Find the cells and give the type of each one.
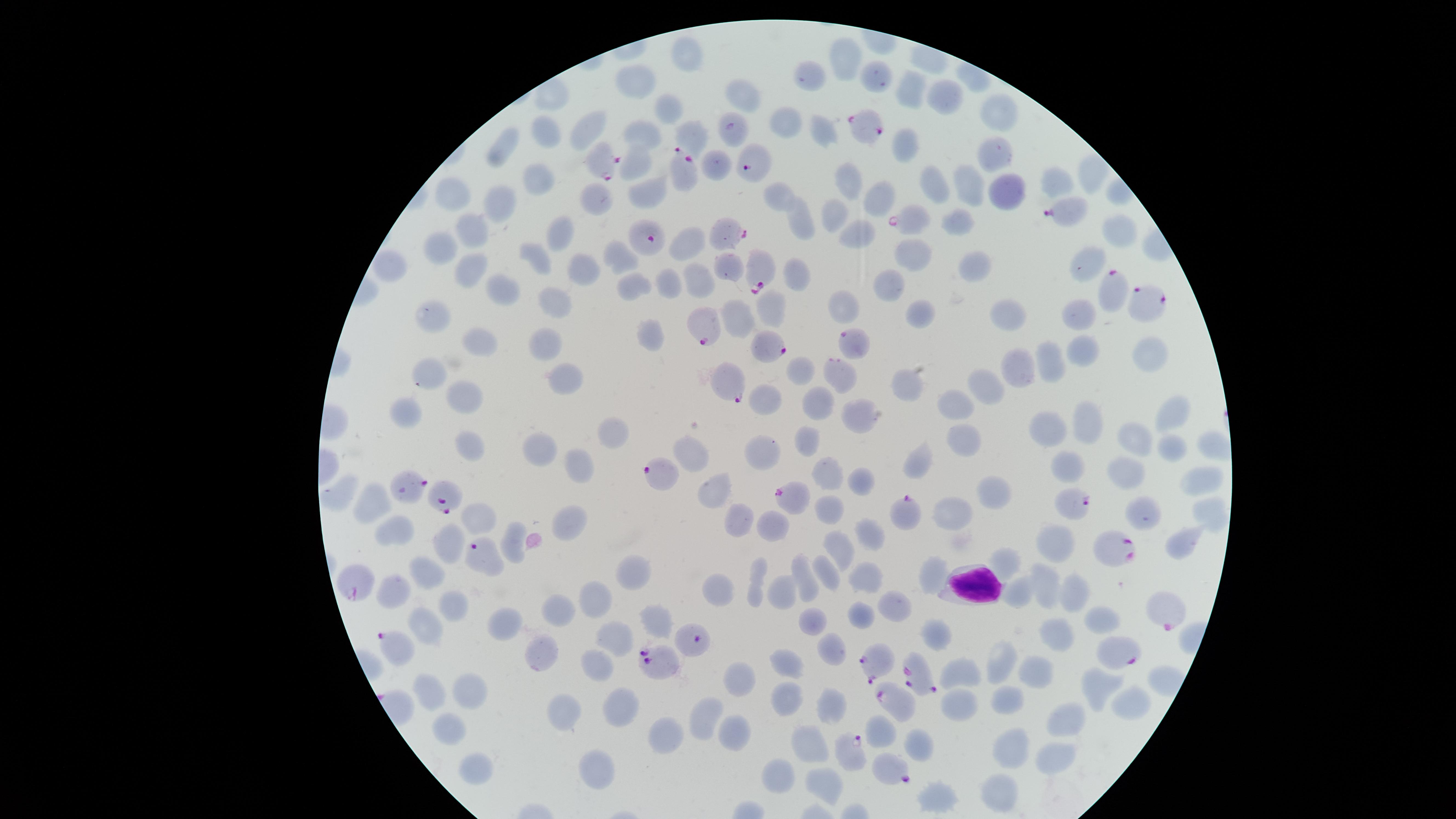

Approximate marker points as {x, y} in pixels.
Parasitized RBCs: {869, 131}, {604, 160}, {752, 164}, {686, 173}, {1066, 211}, {909, 219}, {728, 232}, {647, 238}, {759, 268}, {1111, 295}, {1157, 301}, {707, 328}, {767, 344}, {853, 344}, {838, 368}, {729, 383}, {408, 488}, {789, 495}, {440, 502}, {1072, 505}, {905, 513}, {1113, 550}, {481, 554}, {359, 587}, {1161, 604}, {392, 644}, {1113, 646}, {873, 661}, {656, 662}, {916, 678}, {893, 699}, {847, 744}, {888, 765}.
Uninfected RBCs: {687, 57}, {843, 57}, {870, 75}, {639, 80}, {810, 81}, {908, 94}, {941, 99}, {744, 101}, {669, 107}, {1004, 110}, {786, 124}, {586, 127}, {821, 131}, {643, 134}, {546, 135}, {696, 136}, {902, 145}, {505, 149}, {996, 151}, {639, 158}, {531, 181}, {1056, 181}, {845, 184}, {963, 186}, {930, 188}, {1006, 188}, {646, 191}, {777, 191}, {452, 194}, {596, 198}, {504, 200}, {876, 201}, {833, 215}, {964, 218}, {804, 224}, {475, 229}, {1118, 234}, {558, 236}, {858, 236}, {690, 248}, {440, 249}, {909, 256}, {533, 257}, {615, 257}, {584, 265}, {726, 266}, {976, 266}, {1090, 266}, {394, 268}, {475, 270}, {798, 275}, {701, 279}, {635, 284}, {670, 284}, {891, 284}, {504, 289}, {553, 299}, {843, 305}, {769, 310}, {1082, 312}, {434, 314}, {1001, 314}, {917, 315}, {741, 317}, {479, 340}, {546, 342}, {651, 343}, {1078, 346}, {1144, 354}, {1055, 356}, {802, 367}, {1015, 369}, {425, 372}, {567, 375}, {902, 385}, {988, 386}, {463, 397}, {764, 399}, {956, 399}, {814, 404}, {407, 410}, {858, 413}, {1163, 416}, {1082, 424}, {612, 429}, {1046, 431}, {1130, 435}, {807, 441}, {964, 441}, {1215, 441}, {469, 445}, {1169, 445}, {543, 447}, {761, 454}, {695, 457}, {576, 463}, {915, 466}, {1070, 469}, {1127, 473}, {830, 477}, {1203, 480}, {862, 482}, {714, 493}, {335, 495}, {990, 495}, {376, 507}, {829, 508}, {943, 513}, {473, 515}, {1140, 516}, {1214, 516}, {742, 520}, {574, 522}, {771, 522}, {400, 531}, {873, 536}, {1185, 539}, {513, 540}, {445, 545}, {1054, 545}, {840, 548}, {1006, 563}, {831, 569}, {636, 573}, {424, 574}, {934, 574}, {868, 579}, {758, 582}, {810, 582}, {1043, 584}, {785, 588}, {720, 590}, {397, 592}, {596, 592}, {1019, 593}, {1071, 593}, {893, 605}, {463, 607}, {565, 610}, {1097, 616}, {657, 617}, {862, 617}, {814, 621}, {508, 624}, {423, 626}, {1059, 633}, {613, 634}, {938, 636}, {835, 648}, {545, 653}, {1008, 660}, {788, 661}, {596, 665}, {1037, 668}, {965, 675}, {742, 678}, {1095, 687}, {472, 691}, {788, 693}, {437, 695}, {1131, 702}, {1008, 703}, {627, 706}, {565, 708}, {957, 710}, {829, 713}, {705, 716}, {1068, 720}, {450, 726}, {734, 729}, {881, 731}, {669, 737}, {918, 742}, {1010, 746}, {811, 750}, {1053, 756}, {473, 769}, {592, 771}, {781, 776}, {826, 785}, {937, 792}, {999, 794}.
WBCs: {973, 582}.

Summary:
  - Visible region: circular
  - Image size: 1456×819 pixels
  - Field of view: single
  - Stain: Giemsa
  - Capture: smartphone photograph through the microscope eyepiece
  - Preparation: thin blood film
  - Species: Plasmodium falciparum